Assess the morphology of the erythrocytes.
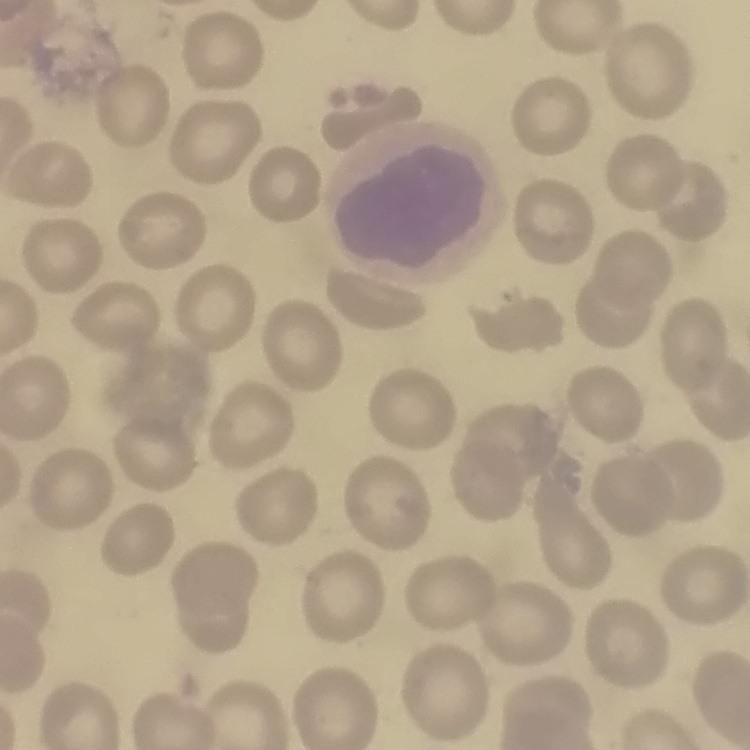

No rouleaux formation.

image type = square crop of a larger photomicrograph
preparation = thin blood smear
stain = Field's or Giemsa